State which cell type is depicted.
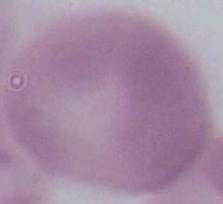
This is an erythrocyte.

Photomicrograph. Captured at 1000x magnification.